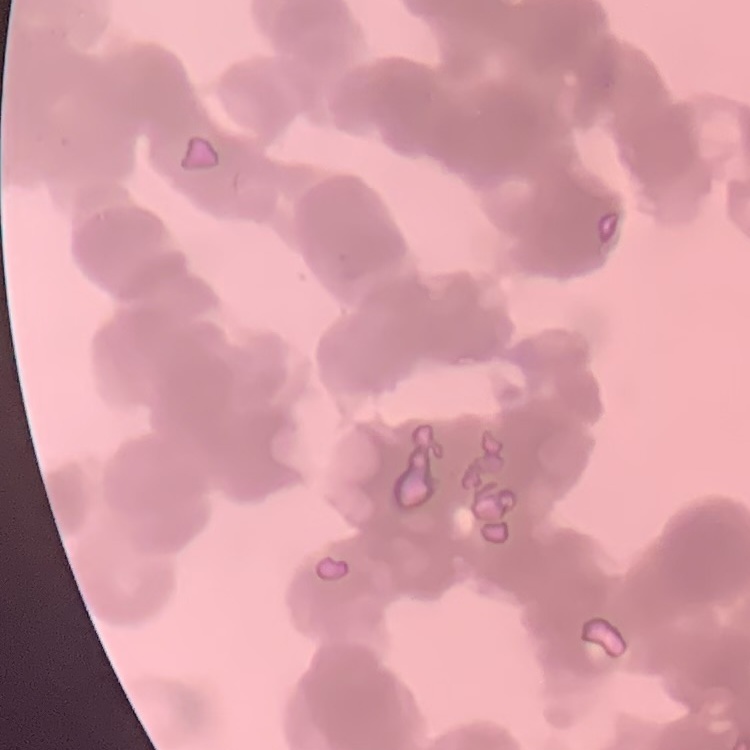
{
  "erythrocyte_morphology": "rouleaux formation",
  "image_type": "square crop of a larger photomicrograph",
  "preparation": "thin peripheral smear",
  "stain": "Field's or Giemsa"
}